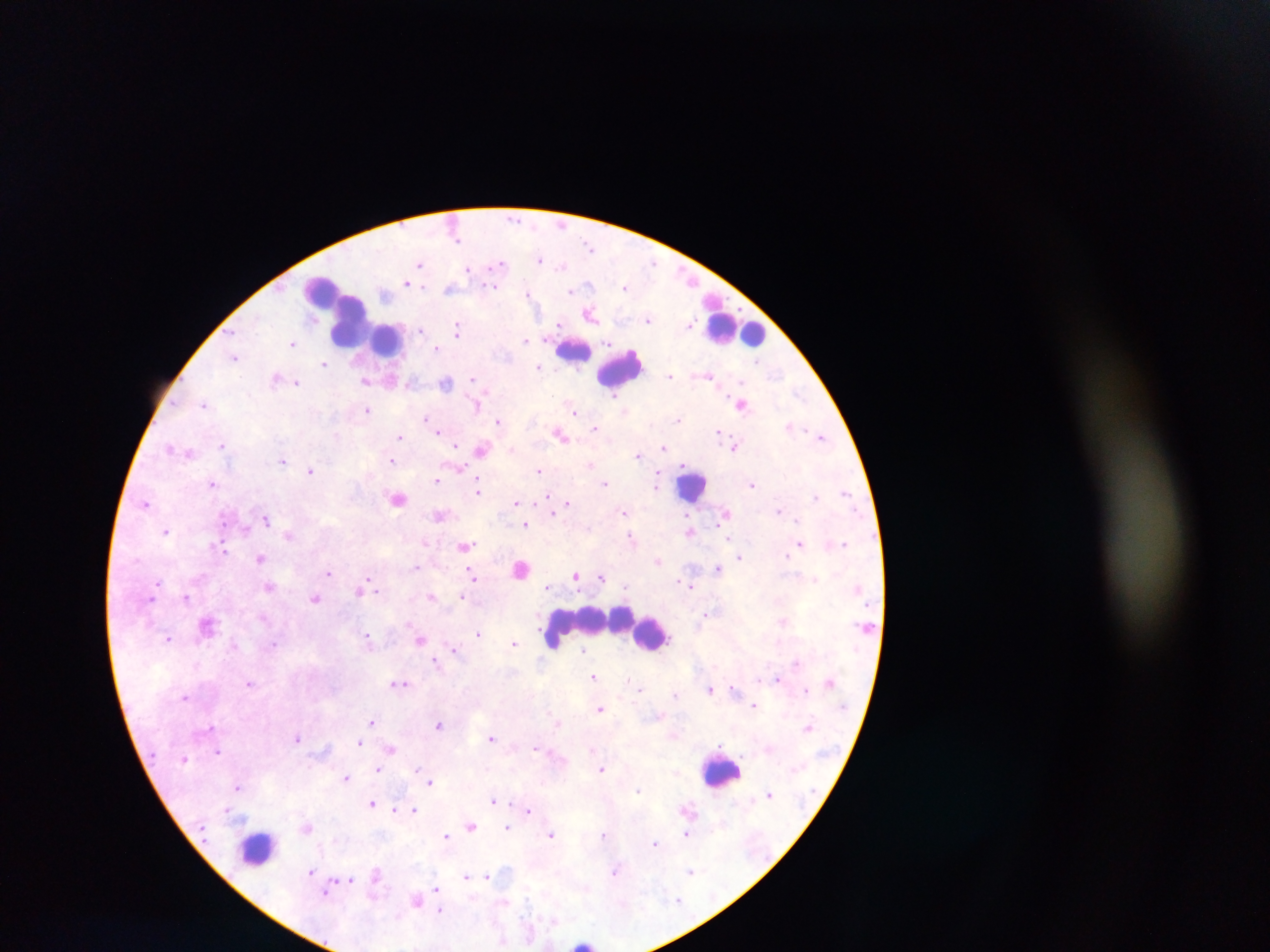
Approximate centers as (x, y) in pixels. Leukocyte locations: (338, 313), (363, 324), (734, 327), (388, 339), (574, 348), (620, 368), (691, 485), (590, 621), (651, 633), (721, 770), (259, 847), (586, 943). Plasmodium parasite locations: (541, 259), (420, 264), (498, 265), (469, 269), (408, 282), (495, 286), (625, 287), (449, 288), (571, 290), (529, 293), (591, 313), (649, 319), (690, 323), (457, 329), (420, 330), (527, 339), (293, 344), (437, 348), (235, 357), (324, 364), (538, 367), (709, 375), (671, 376), (277, 377), (473, 378), (289, 381), (367, 381), (298, 382), (445, 382), (742, 403), (206, 404), (367, 410), (574, 411), (427, 418), (678, 419), (499, 422), (791, 425), (596, 428), (439, 430), (719, 432), (561, 434), (402, 436), (823, 436), (223, 444), (458, 445), (735, 446), (173, 448), (664, 448), (481, 449), (513, 449), (181, 451), (189, 453), (639, 454), (283, 460), (392, 460), (591, 463), (460, 467), (311, 471), (539, 471), (437, 480), (213, 482), (605, 483), (657, 483), (752, 483), (479, 489), (845, 491), (816, 495), (548, 496), (397, 497), (146, 502), (516, 503), (568, 503), (552, 511), (780, 511), (625, 512), (727, 513), (442, 515), (267, 519), (526, 524), (166, 530), (690, 530), (289, 534), (632, 538), (424, 542), (844, 542), (800, 544), (466, 545), (220, 547), (786, 554), (740, 556), (259, 558), (658, 560), (417, 567), (522, 567), (718, 567), (329, 573), (577, 574), (473, 576), (602, 577), (685, 581), (691, 586), (268, 587), (360, 590), (378, 590), (432, 596), (462, 596), (187, 598), (316, 598), (152, 599), (705, 614), (783, 621), (208, 623), (479, 633), (169, 638), (369, 639), (421, 639), (514, 642), (273, 644), (454, 649), (583, 649), (436, 661), (594, 676), (779, 679), (250, 683), (399, 683), (640, 688), (733, 688), (711, 689), (806, 690), (675, 695), (185, 696), (754, 705), (600, 708), (372, 721), (559, 722), (439, 725), (211, 727), (808, 727), (674, 735), (298, 738), (492, 738), (360, 743), (391, 748), (535, 748), (592, 749), (218, 751), (186, 758), (417, 766), (378, 768), (601, 768), (347, 778), (431, 782), (239, 786), (639, 788), (770, 794), (493, 800), (372, 803), (227, 809), (396, 809), (415, 809), (687, 809), (528, 810), (472, 825), (306, 826), (507, 827), (687, 833), (604, 834), (551, 835), (446, 836), (655, 843), (616, 870), (312, 871), (690, 871), (376, 874), (465, 875), (488, 876), (351, 879), (436, 888), (327, 892), (417, 900), (678, 900), (440, 910), (502, 942). Single field of view. Thick blood film. Sample from Ghana. Image is 1270×952 pixels. Photographed through a microscope with a mobile-phone camera.